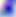
magnification = 400x
modality = photomicrograph
identification = Toxoplasma gondii